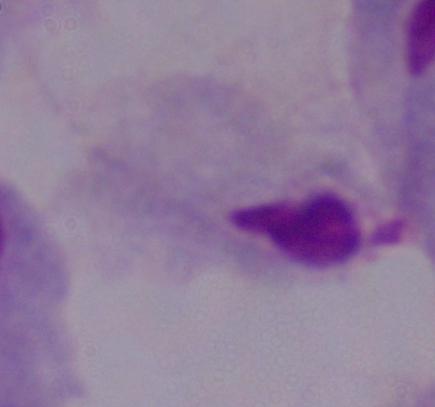 Photomicrograph. A trichomonad is shown. 1000x magnification.